Evaluate for malaria.
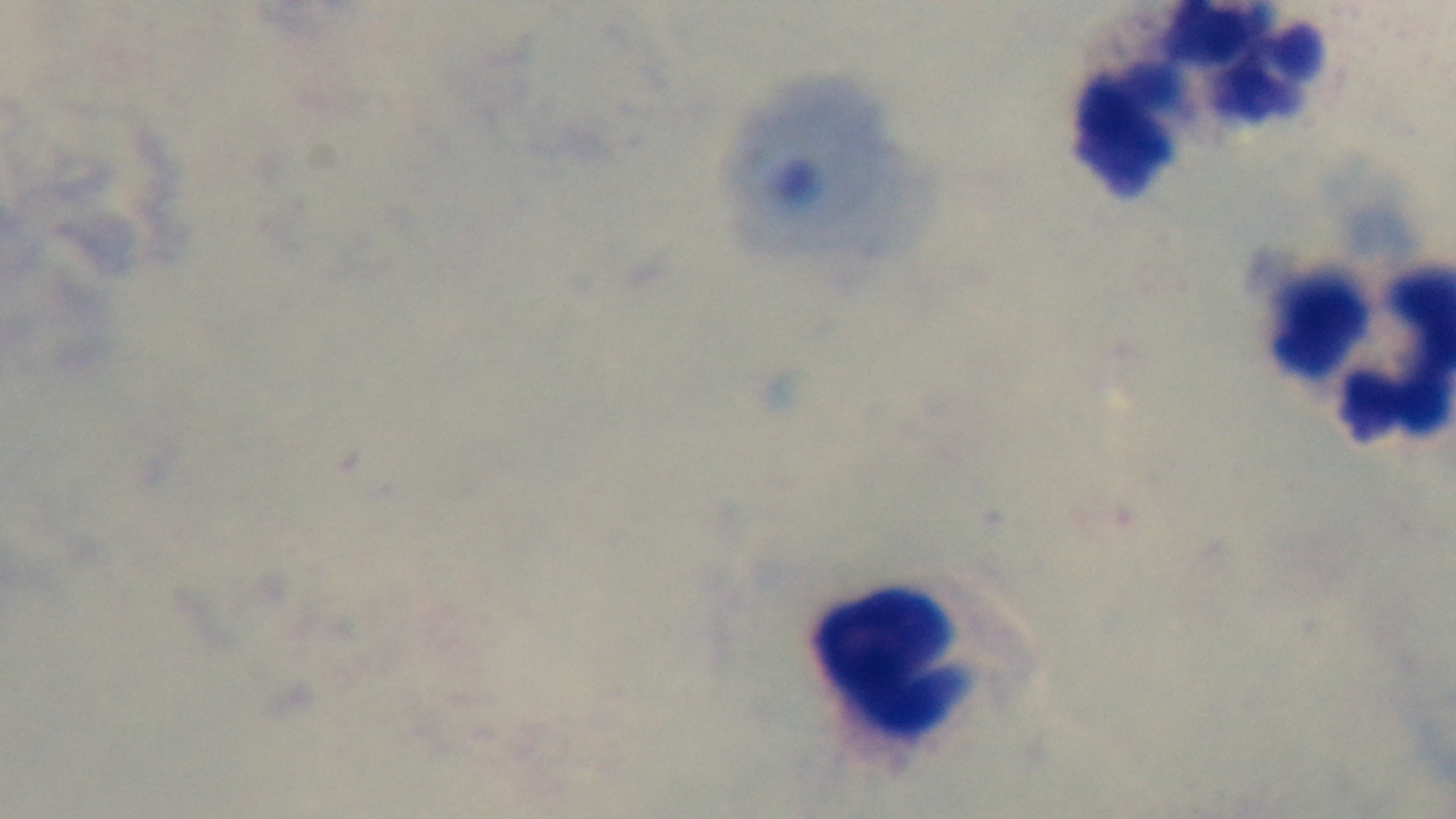
Uninfected.

capture: mounted 4K digital camera
objective: 100x oil immersion
field_of_view: one from the slide
stain: Giemsa
preparation: thick
modality: light microscopy